Classify this cell by malaria status.
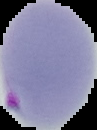

Parasitized.

image type = segmented cell region on a black background
preparation = thin blood film
image size = 97×130 pixels